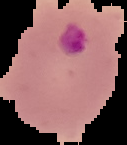
Image is 127×145 pixels. From a thin blood smear. Malaria status: parasitized. The area outside the segmented cell region is set to black.